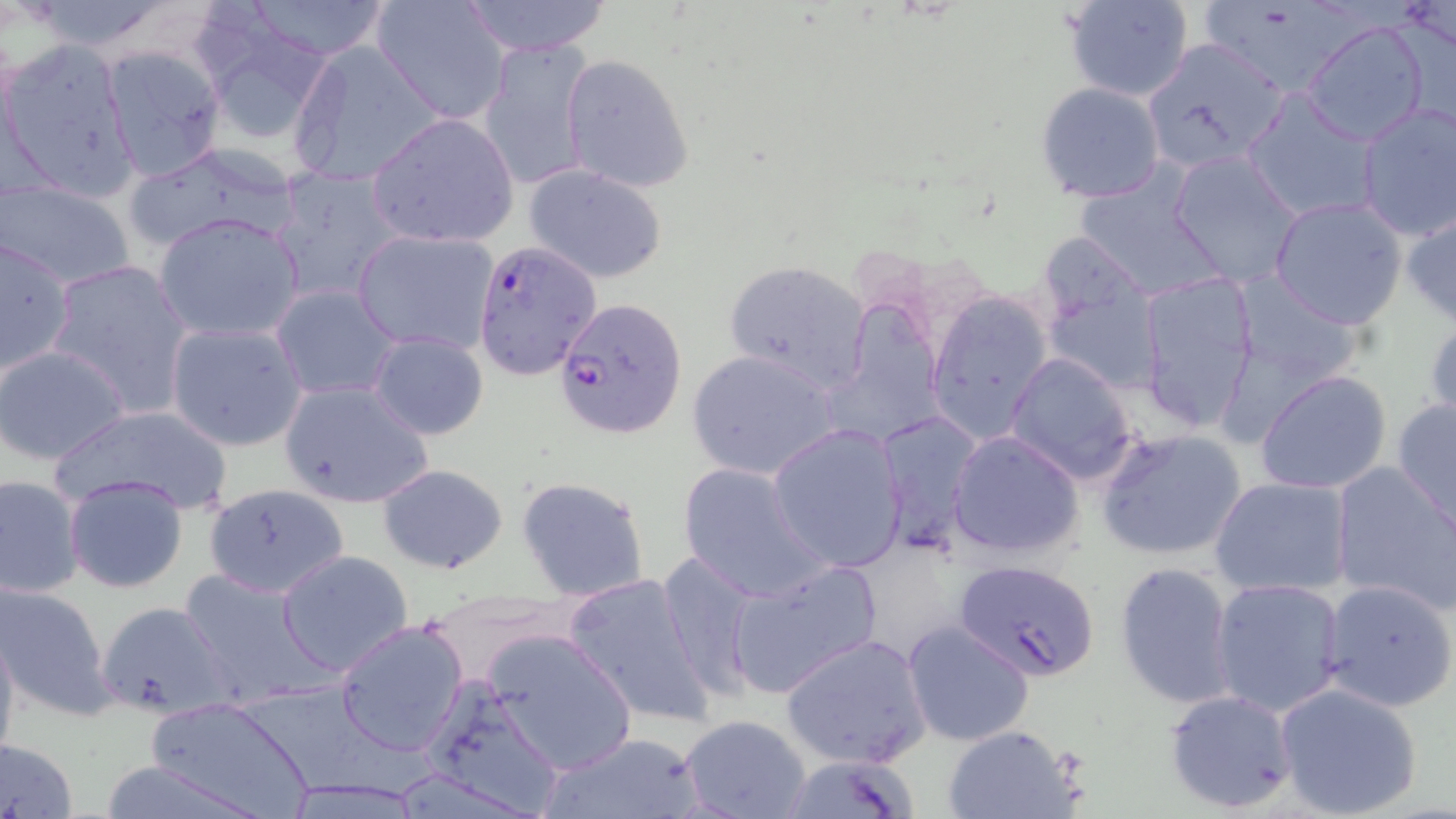

Approximate bounding boxes as (x1, y1, x2, y2) in pixels. Plasmodium falciparum-infected red blood cell locations: (476, 241, 602, 381), (554, 297, 687, 438), (955, 558, 1101, 682). Uninfected red blood cell locations: (23, 0, 175, 56), (242, 0, 392, 61), (372, 0, 510, 123), (459, 0, 612, 56), (1061, 0, 1195, 102), (1198, 0, 1363, 100), (193, 6, 337, 146), (1301, 19, 1431, 146), (477, 37, 598, 190), (1139, 37, 1291, 175), (287, 38, 447, 187), (2, 40, 138, 201), (101, 46, 227, 183), (560, 54, 693, 194), (1036, 82, 1166, 204), (1242, 86, 1378, 219), (1355, 100, 1455, 242), (365, 111, 519, 247), (121, 140, 307, 253), (1168, 151, 1305, 288), (525, 165, 668, 283), (269, 166, 405, 302), (2, 179, 137, 289), (1268, 196, 1409, 330), (1401, 208, 1456, 328), (154, 212, 304, 343), (354, 229, 498, 354), (0, 236, 77, 381), (46, 258, 194, 419), (724, 260, 872, 393), (1136, 269, 1261, 434), (1227, 271, 1366, 386), (1041, 276, 1162, 394), (271, 284, 404, 401), (925, 292, 1053, 445), (833, 301, 948, 447), (1425, 307, 1456, 429), (165, 322, 308, 451), (368, 330, 488, 440), (0, 345, 130, 466), (688, 349, 842, 481), (1006, 351, 1138, 485), (1254, 371, 1392, 496), (278, 379, 435, 508), (1391, 397, 1455, 530), (48, 404, 236, 516), (874, 410, 982, 552), (768, 422, 908, 572), (1096, 427, 1249, 561), (947, 430, 1085, 560), (1328, 459, 1456, 615), (676, 461, 830, 602), (377, 463, 509, 574), (0, 474, 86, 600), (63, 474, 189, 595), (515, 476, 650, 602), (1210, 476, 1353, 597), (204, 483, 350, 599), (278, 550, 413, 677), (654, 550, 764, 700), (723, 558, 884, 699), (1114, 562, 1237, 710), (174, 570, 326, 706), (561, 572, 717, 728), (1209, 578, 1348, 717), (1319, 579, 1456, 714), (0, 581, 117, 721), (419, 588, 572, 683), (98, 601, 234, 719), (336, 618, 469, 756), (0, 620, 21, 768), (904, 621, 1036, 746), (482, 627, 639, 776), (780, 632, 930, 771), (419, 678, 568, 816), (1274, 682, 1425, 819), (1164, 687, 1297, 813), (141, 695, 313, 817), (678, 714, 812, 819), (939, 725, 1082, 819), (541, 733, 705, 819), (0, 737, 78, 819). Slide-level diagnosis: Plasmodium falciparum. May-Grünwald-Giemsa stain. Captured at 1000x magnification. Image is 1456×819 pixels. Optical microscopy. Thin blood film. One field of a larger specimen.